Comment on the morphology of the erythrocytes.
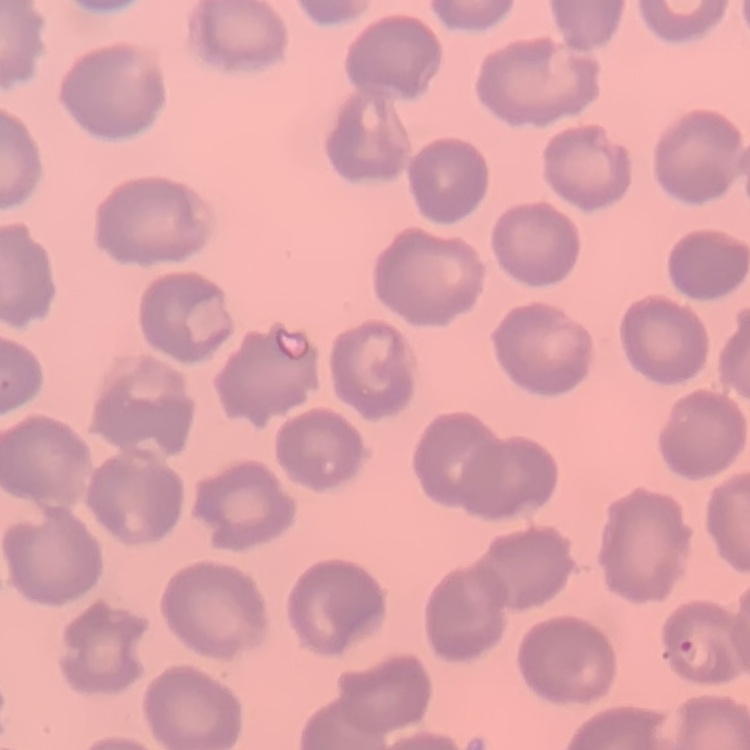

They show no rouleaux formation.

Summary:
  - Preparation: thin blood smear
  - Stain: Field's or Giemsa
  - Image type: one tile cut from a larger photomicrograph